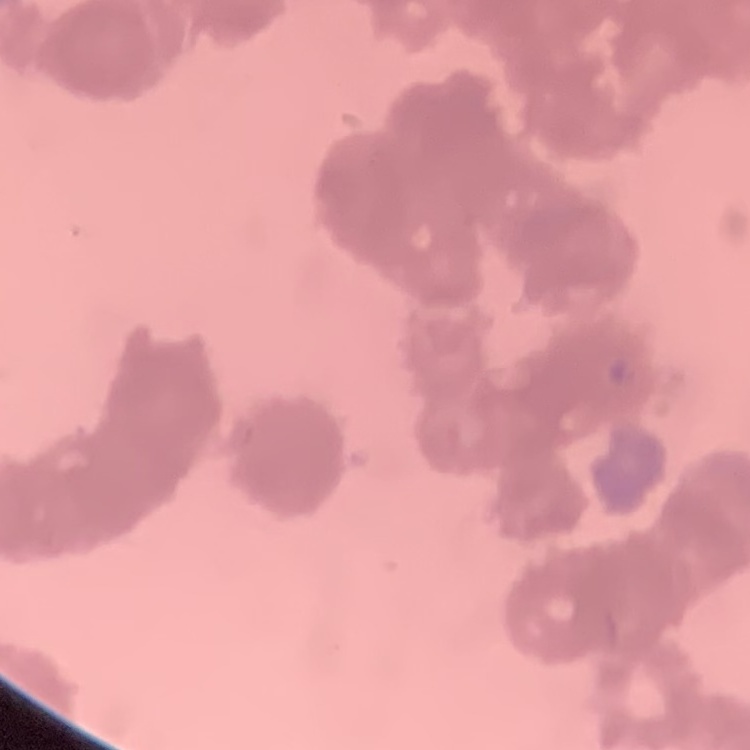 The red blood cells exhibit rouleaux formation. Field's or Giemsa stain. Thin blood smear. One tile cut from a larger photomicrograph.